Assess the morphology of the red blood cells.
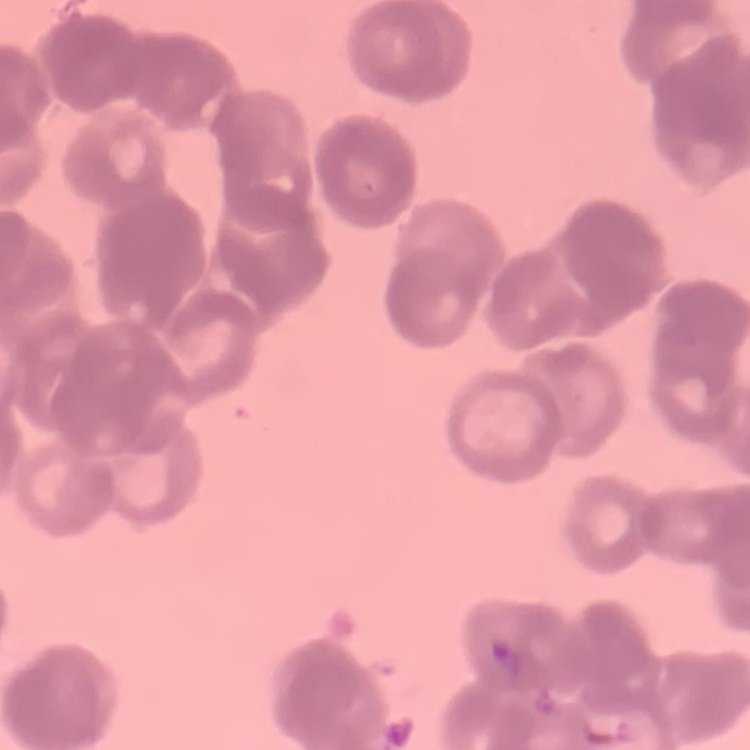

Rouleaux formation.

stain = Field's or Giemsa
preparation = thin peripheral smear
image type = one tile cut from a larger photomicrograph